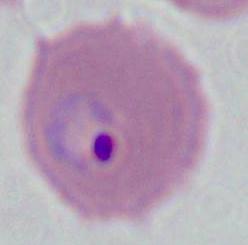

modality = photomicrograph
magnification = 400x or 1000x
identification = Plasmodium